Assess this cell for malaria.
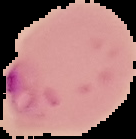
Parasitized.

{
  "image_type": "cell region segmented out of the field of view; surrounding area masked to black",
  "image_size": "136×139 pixels",
  "preparation": "thin blood smear"
}